Assess the morphology of the red blood cells.
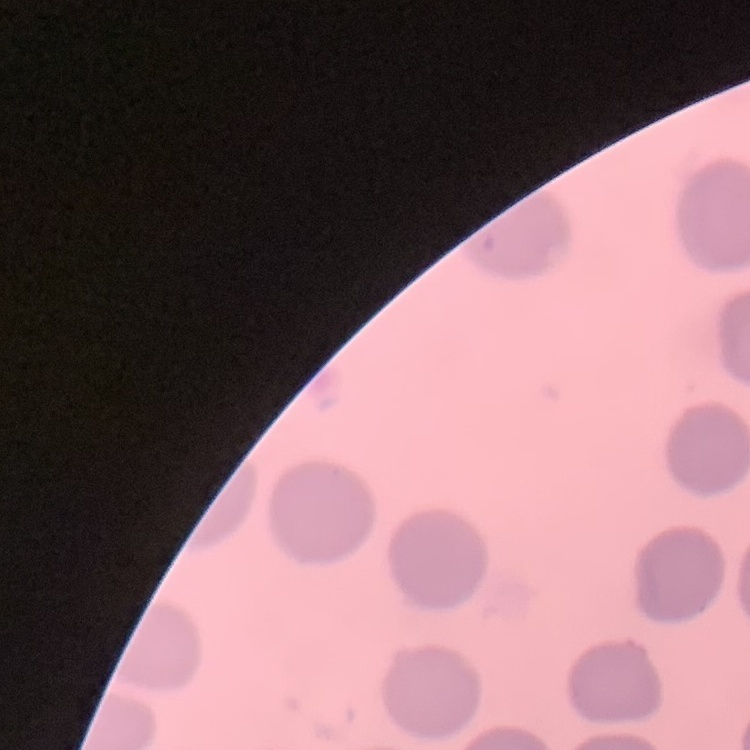

They show no rouleaux formation.

{
  "image_type": "one tile cut from a larger photomicrograph",
  "preparation": "thin blood film",
  "stain": "Field's or Giemsa"
}